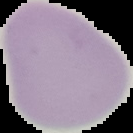
Summary:
  - Image type: cell region segmented out of the field of view; surrounding area masked to black
  - Result: negative for Plasmodium parasites
  - Preparation: thin blood film
  - Image size: 133×133 pixels